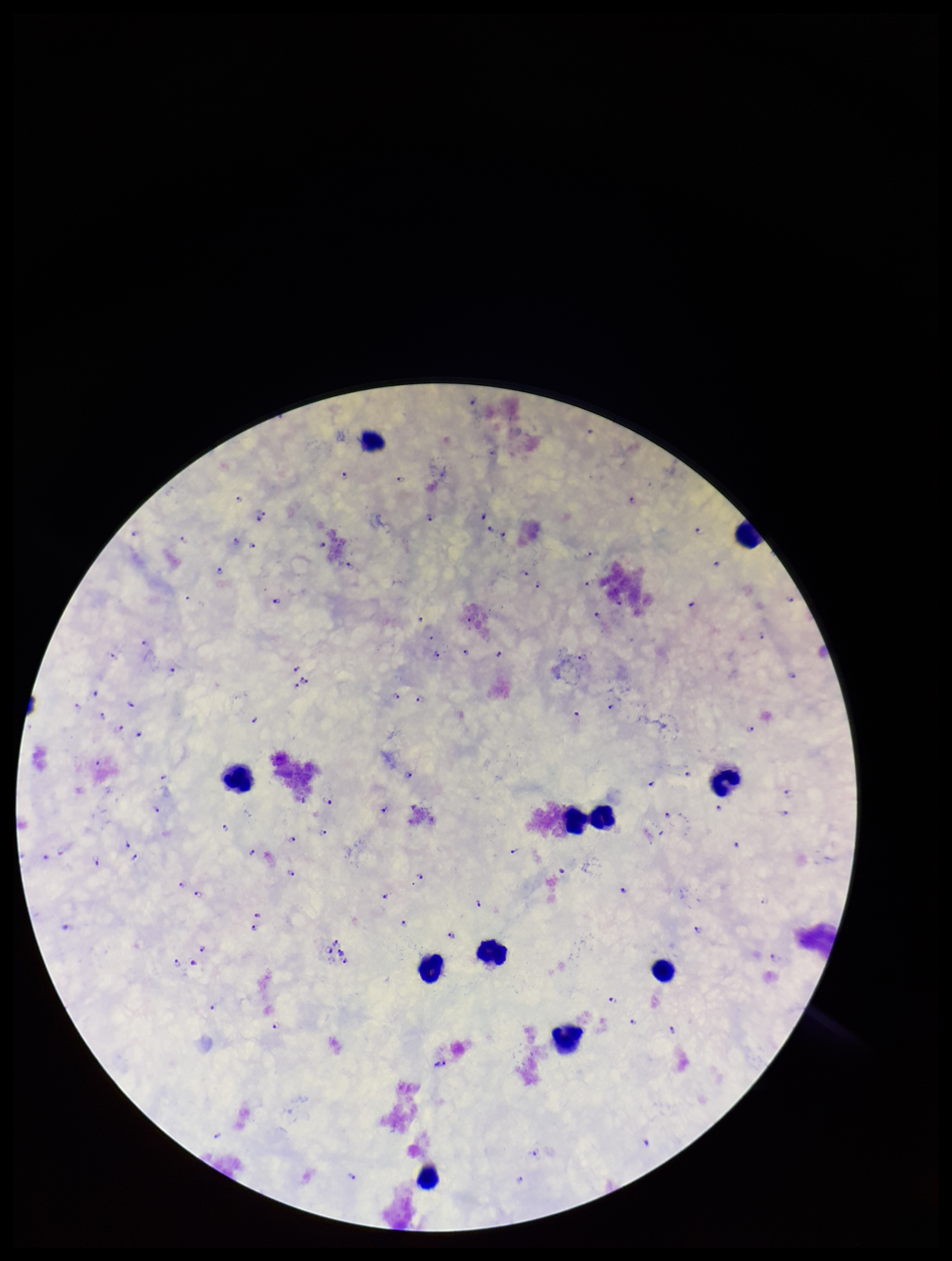
Image is 952×1261 pixels. Patient malaria status: positive. Leukocyte count: 11. Photographed through the microscope eyepiece with a smartphone camera. Species reported for this patient: Plasmodium falciparum. Plasmodium parasites: seen. Preparation: thick. One field from this slide. Parasite count: 120. Giemsa stain.